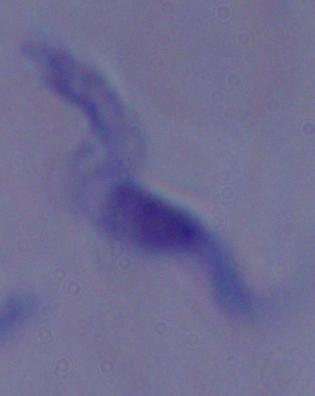
Summary:
  - Magnification: 1000x
  - Identification: trypanosome
  - Modality: photomicrograph